State which parasite is depicted.
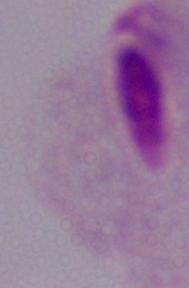
A trichomonad.

magnification = 1000x
modality = photomicrograph